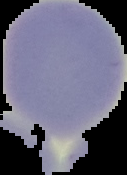
Summary:
  - Result: no malaria parasites seen
  - Image type: cell region segmented out of the field of view; surrounding area masked to black
  - Image size: 127×175 pixels
  - Preparation: thin blood smear